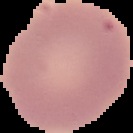

From a thin blood film. Segmented cell region on a black background. Image is 133×133 pixels. Result: negative for malaria parasites.